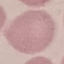

result = no malaria parasites seen
image type = cell patch, automatically extracted from a larger field of view and resized to 64 × 64 pixels
capture = smartphone camera at the microscope eyepiece
preparation = thin blood film
stain = Giemsa